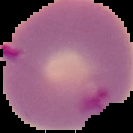
Summary:
  - Image size: 133×133 pixels
  - Result: Plasmodium parasites detected
  - Preparation: thin blood smear
  - Image type: cell region segmented out of the field of view; surrounding area masked to black